Name the parasite shown.
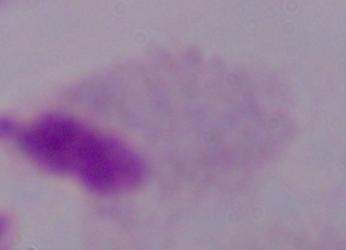
A trichomonad.

Micrograph. Captured at 1000x magnification.